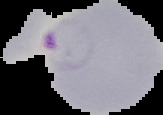 Result: Plasmodium parasites identified. From a thin blood smear. Cell region segmented out of the field of view; the surrounding area is masked to black. Image is 163×115 pixels.